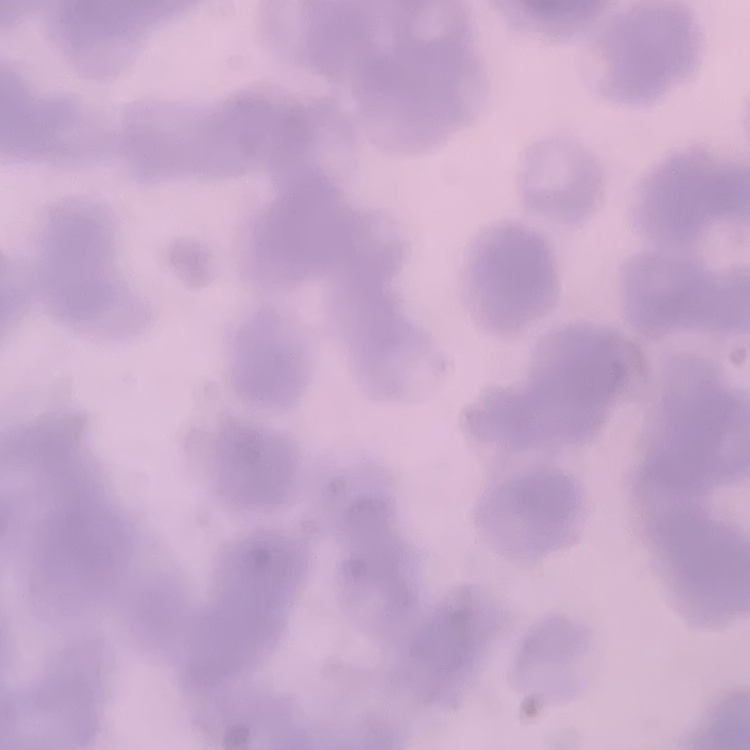

Summary:
  - Red blood cell morphology: rouleaux formation
  - Stain: Field's or Giemsa
  - Preparation: thin peripheral smear
  - Image type: one tile cut from a larger photomicrograph